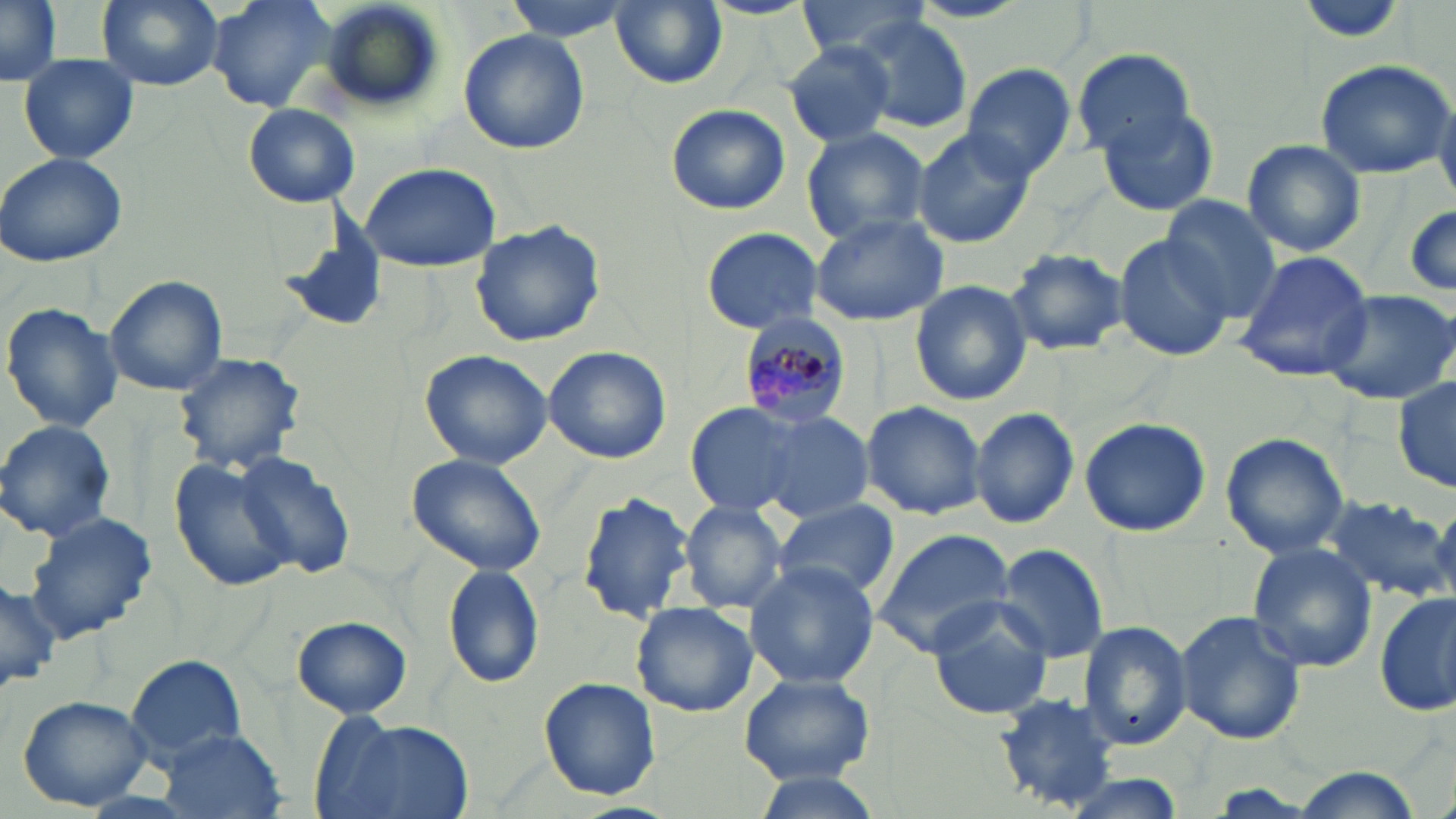

Summary:
  - Coordinate format: approximate bounding boxes as (x1, y1, x2, y2) in pixels
  - Uninfected red blood cell locations: (1, 0, 63, 86), (96, 0, 225, 91), (204, 0, 339, 112), (319, 0, 447, 112), (503, 0, 631, 40), (610, 0, 727, 89), (792, 0, 935, 59), (852, 14, 975, 133), (457, 28, 589, 156), (782, 40, 899, 148), (1072, 47, 1197, 157), (19, 54, 139, 164), (1315, 59, 1452, 178), (961, 65, 1077, 181), (1433, 87, 1456, 206), (243, 103, 361, 207), (665, 103, 790, 215), (1099, 105, 1220, 217), (801, 126, 931, 247), (911, 126, 1033, 249), (1241, 139, 1366, 257), (0, 152, 130, 267), (360, 162, 500, 272), (1173, 166, 1332, 297), (1160, 195, 1282, 320), (1405, 199, 1456, 302), (271, 203, 394, 337), (808, 211, 951, 326), (470, 218, 606, 347), (700, 225, 826, 335), (1112, 232, 1238, 364), (1004, 247, 1128, 356), (1233, 250, 1375, 382), (103, 276, 226, 396), (910, 280, 1033, 406), (1318, 288, 1456, 406), (1, 303, 123, 433), (543, 346, 672, 463), (419, 349, 553, 468), (173, 350, 309, 474), (1394, 375, 1455, 495), (684, 400, 816, 516), (860, 400, 988, 520), (970, 406, 1079, 530), (752, 408, 876, 522), (1079, 417, 1211, 538), (0, 419, 117, 542), (1219, 432, 1349, 560), (233, 453, 356, 578), (406, 453, 548, 576), (167, 457, 296, 594), (577, 492, 696, 620), (1322, 494, 1450, 601), (680, 499, 790, 614), (772, 499, 900, 600), (1428, 502, 1456, 606), (23, 510, 157, 644), (869, 528, 1016, 658), (994, 542, 1109, 662), (1246, 542, 1379, 673), (743, 561, 881, 689), (442, 564, 545, 689), (0, 576, 58, 695), (1375, 591, 1455, 718), (926, 598, 1055, 721), (631, 601, 759, 718), (1175, 610, 1307, 745), (292, 615, 411, 720), (1077, 620, 1193, 753), (125, 653, 248, 763), (740, 672, 874, 784), (540, 679, 660, 800), (991, 693, 1130, 814), (16, 695, 154, 811), (317, 717, 475, 818), (156, 727, 286, 817), (1290, 769, 1424, 819), (749, 771, 883, 818), (1053, 774, 1188, 819)
  - Plasmodium malariae-infected red blood cell locations: (736, 313, 854, 428)
  - Slide-level diagnosis: Plasmodium malariae
  - Stain: May-Grünwald-Giemsa
  - Modality: light microscopy
  - Field of view: single
  - Preparation: thin blood film
  - Image size: 1456×819 pixels
  - Magnification: 1000x